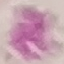
Result: no malaria parasites seen. Cell patch, automatically extracted from a larger field of view and resized to 64 × 64 pixels. Giemsa-stained preparation. Photographed with a smartphone camera at the microscope eyepiece. Thin blood film.